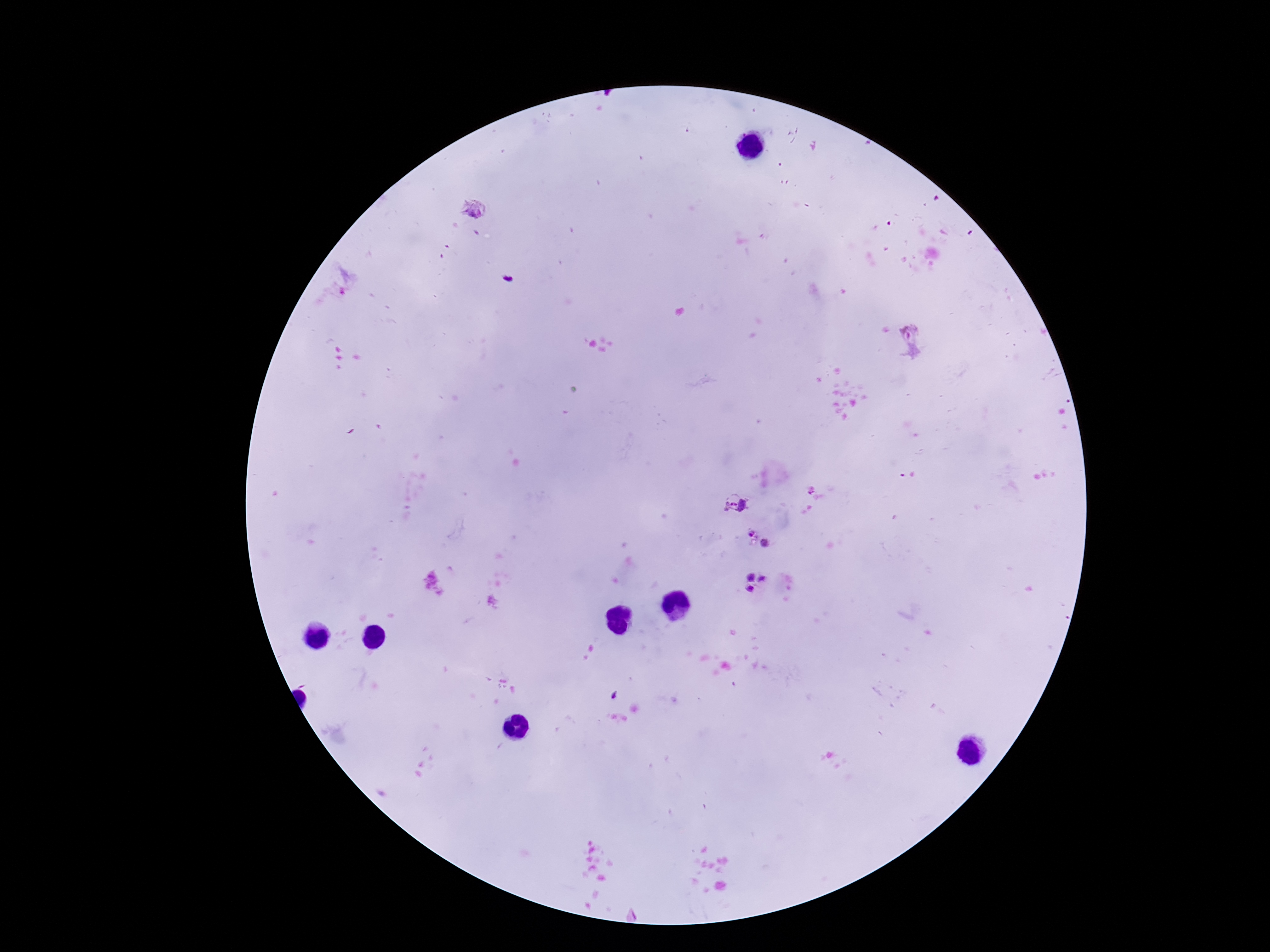
magnification: 100x
patient_malaria_status: infected
field_of_view: one from this slide
plasmodium_parasite_locations: 'approximate centers as [x, y] in pixels: [473, 208], [345, 281], [910, 341], [734, 504], [749, 534], [765, 544], [751, 578], [762, 579], [750, 589]'
capture: smartphone camera through the microscope eyepiece
image_size: 1270×952 pixels
preparation: thick blood smear
stain: Giemsa